Point out each Plasmodium parasite.
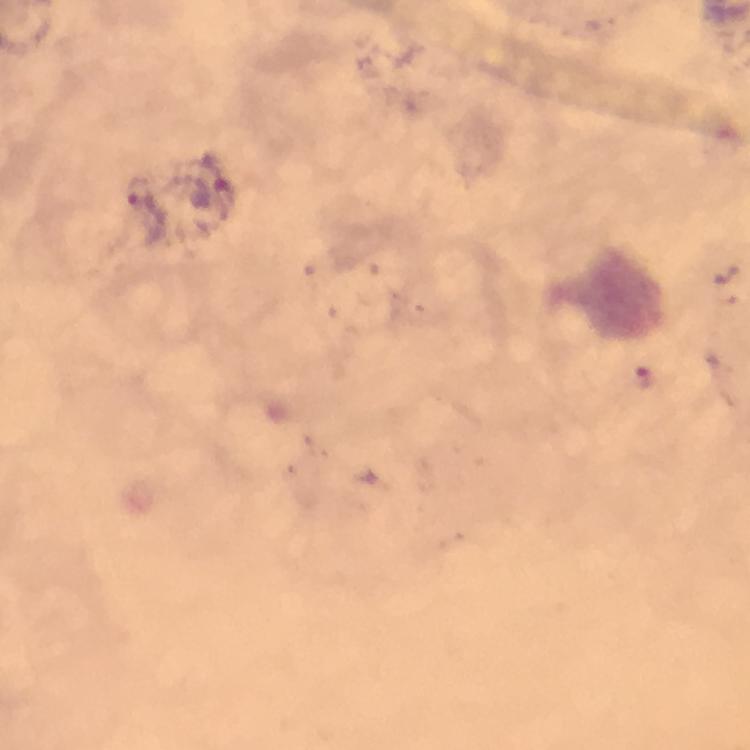
Approximate centers as [x, y] in pixels.
Plasmodium parasites: [140, 191], [644, 377].

Image is 750×750 pixels. Thick smear. Immersion oil was used. Photographed with a smartphone mounted on the microscope. Giemsa-stained preparation. A crop from one field of view. From a diagnostic examination for malaria. 100x magnification.